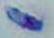

Micrograph. Captured at 1000x magnification. Toxoplasma gondii is seen.